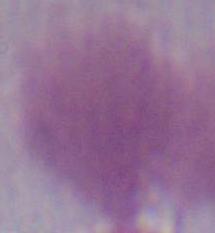

identification: erythrocyte
magnification: 1000x
modality: micrograph